Report the malaria status of this cell.
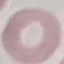
Uninfected.

Thin smear of blood. Automatically extracted cell patch, resized to 64 × 64 pixels. Acquired by smartphone through the microscope eyepiece. Giemsa stain.